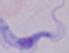
Summary:
  - Identification: trypanosome
  - Modality: micrograph
  - Magnification: 1000x